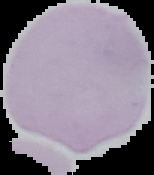

Summary:
  - Image type: segmented cell region with the area outside set to black
  - Result: negative for Plasmodium parasites
  - Image size: 154×175 pixels
  - Preparation: thin blood smear